Give the preparation type.
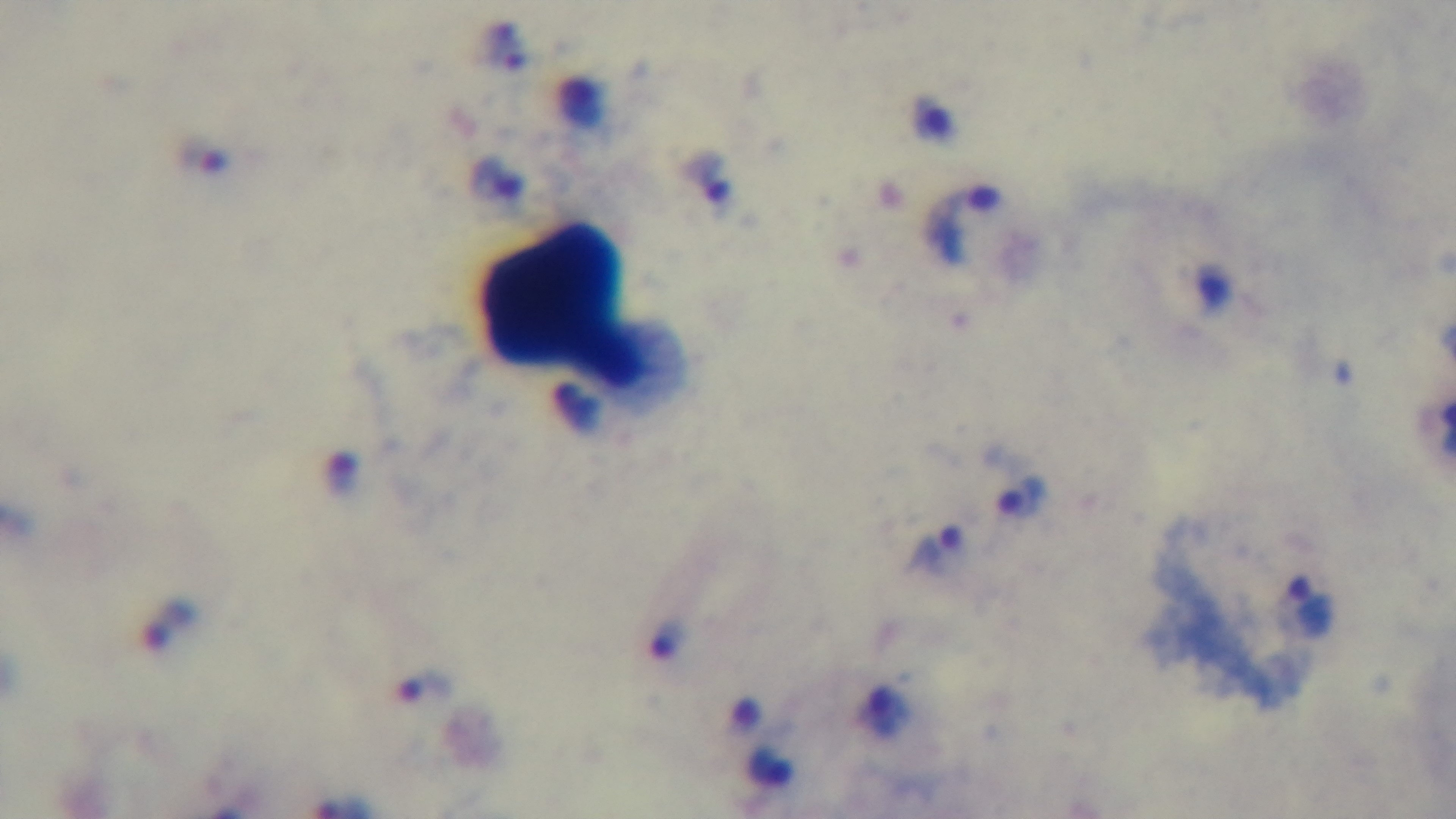

It is a thick blood film.

Summary:
  - Field of view: single
  - Stain: Giemsa
  - Objective: 100x oil immersion
  - Modality: light microscopy
  - Malaria status: positive
  - Capture: mounted 4K digital camera